Classify this cell by malaria status.
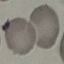
It is uninfected.

Thin blood smear. Acquired by smartphone through the microscope eyepiece. Cell patch, automatically extracted from a larger field of view and resized to 64 × 64 pixels. Giemsa stain.